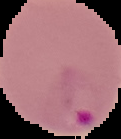 Malaria status: parasitized. From a thin blood film. Image is 121×139 pixels. Cell region segmented out of the field of view; the surrounding area is masked to black.